Give the extent of all Plasmodium falciparum-infected red blood cells.
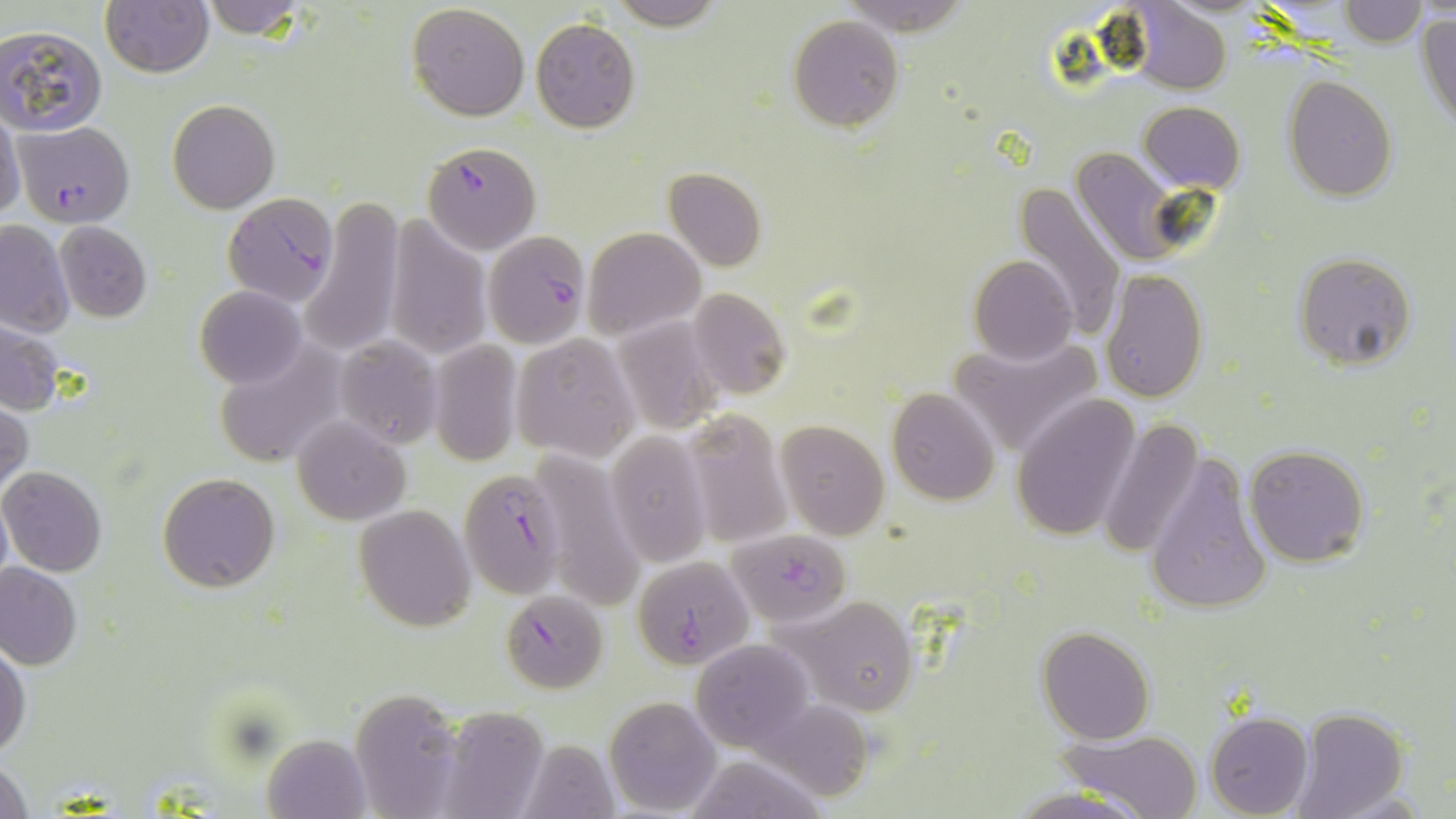

Approximate bounding boxes as named x1/y1/x2/y2 corners in pixels.
Plasmodium falciparum-infected red blood cells: (x1=13, y1=121, x2=134, y2=228), (x1=421, y1=141, x2=540, y2=252), (x1=225, y1=190, x2=337, y2=313), (x1=482, y1=230, x2=592, y2=347), (x1=456, y1=463, x2=573, y2=599), (x1=728, y1=528, x2=853, y2=624), (x1=632, y1=556, x2=753, y2=669), (x1=500, y1=590, x2=609, y2=693).

slide-level diagnosis = Plasmodium falciparum
field of view = single
image size = 1456×819 pixels
modality = optical microscopy
stain = May-Grünwald-Giemsa
uninfected red blood cell locations = approximate bounding boxes as named x1/y1/x2/y2 corners in pixels: (x1=196, y1=0, x2=315, y2=40), (x1=605, y1=0, x2=728, y2=31), (x1=1340, y1=0, x2=1426, y2=46), (x1=101, y1=1, x2=213, y2=77), (x1=407, y1=3, x2=530, y2=120), (x1=1126, y1=3, x2=1231, y2=93), (x1=1416, y1=11, x2=1456, y2=132), (x1=789, y1=15, x2=904, y2=130), (x1=531, y1=19, x2=640, y2=133), (x1=0, y1=26, x2=107, y2=136), (x1=1283, y1=76, x2=1397, y2=202), (x1=167, y1=100, x2=279, y2=214), (x1=1139, y1=100, x2=1245, y2=194), (x1=0, y1=112, x2=25, y2=221), (x1=1070, y1=145, x2=1185, y2=268), (x1=663, y1=167, x2=765, y2=270), (x1=1014, y1=182, x2=1123, y2=339), (x1=302, y1=197, x2=402, y2=353), (x1=384, y1=217, x2=491, y2=360), (x1=0, y1=220, x2=74, y2=337), (x1=54, y1=222, x2=153, y2=322), (x1=581, y1=227, x2=704, y2=340), (x1=1292, y1=252, x2=1416, y2=370), (x1=969, y1=256, x2=1078, y2=365), (x1=1100, y1=269, x2=1208, y2=404), (x1=195, y1=285, x2=307, y2=389), (x1=687, y1=289, x2=790, y2=400), (x1=612, y1=315, x2=721, y2=434), (x1=0, y1=322, x2=65, y2=415), (x1=334, y1=335, x2=442, y2=447), (x1=510, y1=335, x2=638, y2=460), (x1=950, y1=335, x2=1105, y2=457), (x1=429, y1=339, x2=522, y2=465), (x1=214, y1=343, x2=350, y2=469), (x1=886, y1=388, x2=1001, y2=505), (x1=1011, y1=395, x2=1141, y2=543), (x1=0, y1=400, x2=32, y2=498), (x1=682, y1=410, x2=792, y2=547), (x1=293, y1=416, x2=408, y2=523), (x1=1098, y1=418, x2=1204, y2=560), (x1=775, y1=420, x2=890, y2=538), (x1=606, y1=430, x2=713, y2=569), (x1=1244, y1=443, x2=1370, y2=567), (x1=530, y1=446, x2=646, y2=613), (x1=1144, y1=450, x2=1273, y2=617), (x1=0, y1=466, x2=106, y2=576), (x1=157, y1=473, x2=280, y2=593), (x1=0, y1=492, x2=13, y2=593), (x1=354, y1=504, x2=474, y2=630), (x1=0, y1=563, x2=82, y2=669), (x1=784, y1=595, x2=920, y2=714), (x1=1037, y1=626, x2=1154, y2=744), (x1=695, y1=637, x2=812, y2=748), (x1=0, y1=641, x2=30, y2=759), (x1=353, y1=689, x2=470, y2=817), (x1=604, y1=695, x2=723, y2=814), (x1=758, y1=697, x2=876, y2=803), (x1=439, y1=705, x2=548, y2=819), (x1=1288, y1=707, x2=1410, y2=819), (x1=1205, y1=712, x2=1313, y2=819), (x1=1061, y1=731, x2=1202, y2=816), (x1=262, y1=735, x2=368, y2=819), (x1=518, y1=738, x2=619, y2=817), (x1=684, y1=755, x2=828, y2=819), (x1=1, y1=757, x2=32, y2=818), (x1=1004, y1=787, x2=1152, y2=819)
magnification = 1000x
preparation = thin blood smear